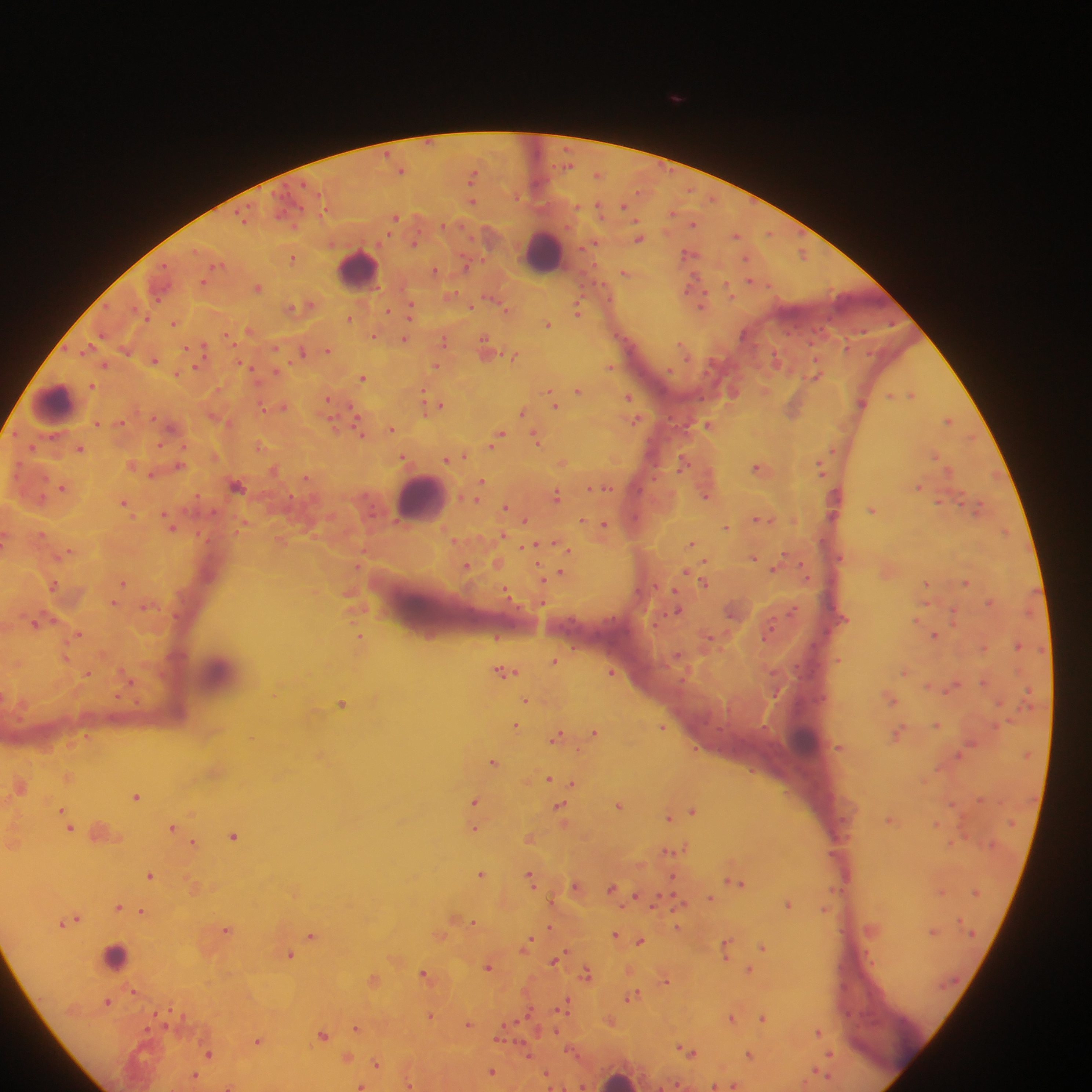
field_of_view: single
country: Ghana
preparation: thick blood film
leukocyte_locations: 'approximate centers as [x, y] in pixels: [544, 250], [357, 269], [54, 402], [420, 498], [220, 672], [806, 740], [114, 956], [619, 1078]'
image_size: 1092×1092 pixels
malaria_parasite_locations: 'approximate centers as [x, y] in pixels: [676, 97], [401, 170], [598, 174], [472, 176], [472, 200], [624, 206], [395, 217], [693, 222], [736, 235], [639, 238], [414, 242], [689, 253], [803, 253], [293, 257], [434, 270], [625, 272], [750, 280], [204, 282], [257, 287], [695, 292], [700, 301], [304, 306], [471, 306], [410, 309], [507, 309], [578, 309], [388, 310], [351, 318], [174, 323], [547, 324], [250, 330], [227, 335], [373, 336], [404, 339], [444, 341], [487, 347], [189, 348], [202, 348], [683, 348], [329, 349], [301, 351], [515, 354], [154, 359], [245, 364], [105, 365], [437, 366], [610, 366], [818, 374], [364, 378], [92, 384], [578, 390], [733, 391], [911, 393], [553, 396], [628, 397], [328, 400], [862, 402], [554, 404], [435, 405], [283, 406], [263, 407], [793, 408], [522, 411], [950, 419], [636, 420], [98, 423], [120, 423], [709, 424], [173, 427], [360, 428], [391, 428], [499, 435], [537, 437], [495, 442], [161, 445], [259, 445], [80, 448], [937, 455], [463, 456], [404, 457], [455, 457], [447, 459], [564, 461], [684, 462], [180, 464], [132, 465], [821, 467], [761, 468], [274, 469], [153, 475], [481, 482], [237, 485], [919, 485], [604, 486], [64, 487], [593, 487], [557, 495], [706, 496], [125, 503], [505, 507], [978, 507], [872, 509], [760, 518], [525, 519], [584, 520], [171, 523], [604, 523], [726, 526], [1005, 530], [502, 535], [691, 543], [535, 545], [568, 550], [67, 552], [754, 556], [777, 565], [466, 566], [562, 573], [543, 578], [704, 581], [124, 582], [967, 582], [927, 583], [53, 584], [506, 592], [350, 593], [114, 602], [990, 602], [145, 607], [678, 610], [955, 612], [38, 622], [770, 631], [77, 633], [934, 634], [361, 637], [497, 637], [1018, 645], [65, 657], [555, 661], [505, 671], [905, 671], [612, 672], [87, 673], [131, 680], [984, 682], [953, 686], [891, 698], [527, 700], [342, 704], [936, 724], [516, 726], [663, 726], [595, 732], [898, 734], [87, 736], [557, 736], [494, 761], [69, 777], [549, 779], [573, 783], [20, 785], [137, 795], [475, 800], [620, 805], [561, 809], [693, 810], [64, 813], [669, 816], [892, 819], [70, 826], [174, 827], [475, 828], [102, 832], [235, 835], [530, 837], [193, 843], [675, 850], [481, 873], [151, 875], [532, 878], [736, 881], [577, 886], [613, 888], [637, 896], [710, 898], [679, 902], [789, 903], [119, 906], [143, 911], [457, 918], [73, 919], [474, 923], [550, 927], [678, 927], [228, 929], [615, 934], [313, 935], [440, 935], [640, 940], [527, 943], [726, 947], [763, 947], [290, 954], [555, 960], [489, 966], [749, 969], [587, 973], [425, 974], [374, 978], [666, 979], [134, 992], [634, 995], [108, 1002], [567, 1003], [430, 1016], [732, 1018], [763, 1018], [610, 1021], [469, 1024], [358, 1027], [818, 1031], [324, 1035], [501, 1035], [258, 1040], [688, 1051], [209, 1054], [831, 1054], [750, 1055], [348, 1058], [377, 1064], [492, 1071], [195, 1075], [547, 1075], [410, 1084], [735, 1084], [361, 1085], [229, 1086], [715, 1086]'
capture: mobile-phone photograph through a microscope